Assess this cell for malaria.
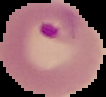

Parasitized.

Summary:
  - Image size: 106×97 pixels
  - Preparation: thin blood smear
  - Image type: cell region segmented out of the field of view; surrounding area masked to black